Give the position of every malaria parasite and every leukocyte.
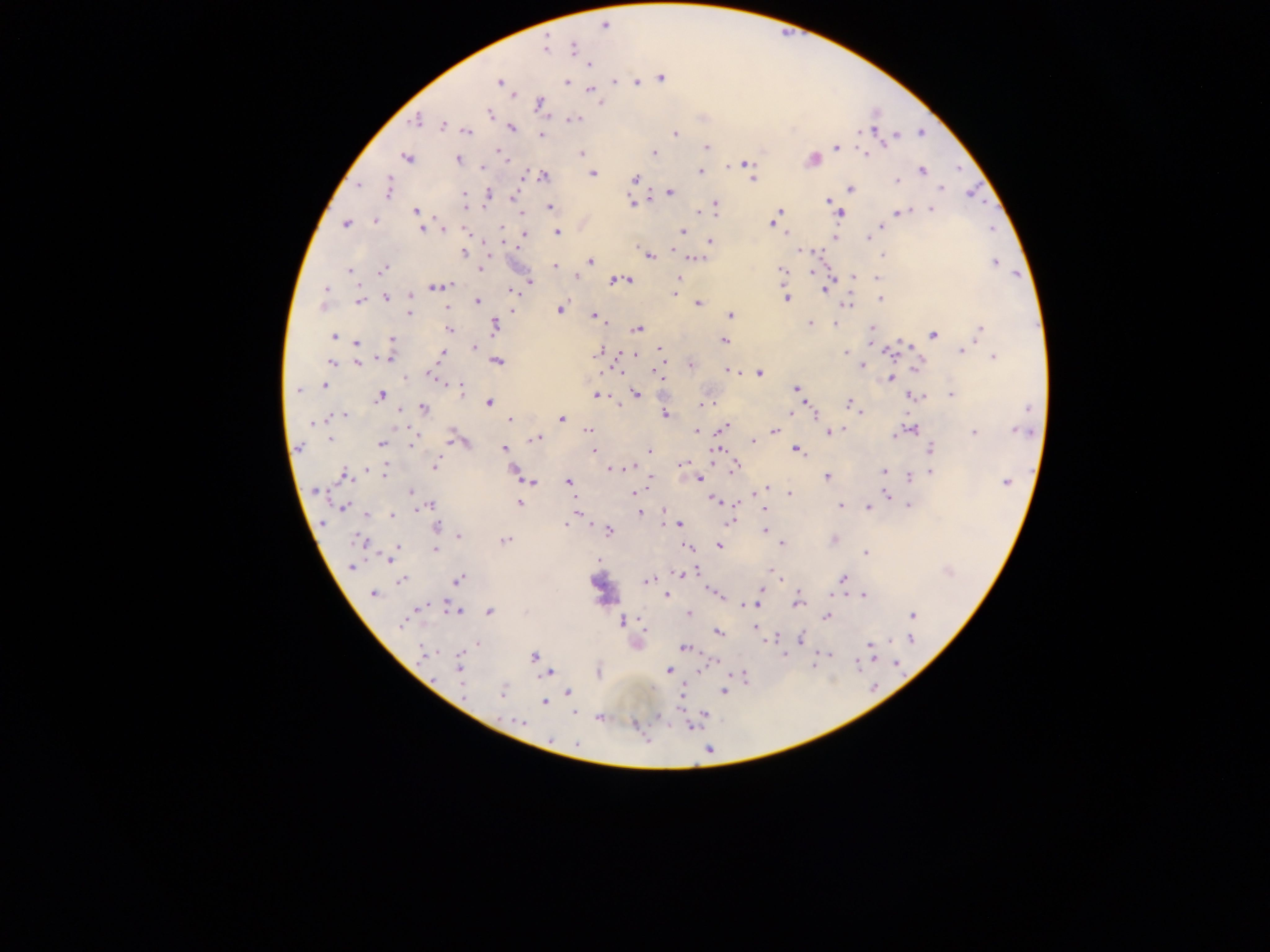
Approximate centers as x y in pixels.
Malaria parasites: 603 26; 546 48; 574 48; 590 64; 661 78; 499 82; 615 82; 639 82; 567 83; 592 91; 513 94; 539 103; 601 103; 489 113; 416 120; 572 120; 442 125; 512 128; 467 131; 921 133; 675 134; 541 136; 895 136; 706 147; 836 148; 500 153; 582 153; 654 153; 865 153; 505 157; 407 158; 457 159; 812 159; 507 161; 745 164; 482 168; 700 172; 921 172; 592 174; 544 177; 635 179; 751 179; 897 180; 359 184; 941 188; 387 189; 850 189; 670 192; 489 195; 465 196; 514 197; 827 201; 466 203; 632 203; 715 204; 550 207; 931 210; 417 211; 699 213; 900 213; 521 214; 778 214; 841 214; 375 221; 773 222; 346 224; 882 226; 502 228; 422 229; 444 230; 466 231; 683 231; 558 232; 524 234; 868 238; 835 239; 711 241; 801 251; 465 253; 883 255; 649 256; 695 258; 486 260; 589 261; 995 263; 556 266; 482 269; 383 270; 782 270; 350 271; 813 272; 576 277; 854 277; 678 278; 877 278; 625 279; 529 281; 614 281; 437 287; 327 288; 677 288; 825 289; 520 291; 416 292; 515 292; 410 296; 386 297; 787 298; 881 300; 359 301; 477 301; 698 304; 848 304; 322 306; 447 308; 560 309; 409 313; 730 315; 594 316; 602 322; 811 323; 835 324; 495 326; 449 329; 872 329; 981 329; 637 330; 933 335; 334 336; 392 338; 725 341; 356 343; 474 347; 660 349; 962 351; 599 352; 845 352; 442 354; 629 354; 635 354; 662 356; 390 357; 994 357; 498 361; 331 363; 358 363; 691 365; 862 366; 657 372; 730 372; 759 373; 430 377; 407 378; 891 379; 324 386; 461 388; 796 389; 298 390; 636 393; 951 395; 381 396; 598 396; 915 396; 489 403; 850 403; 702 405; 853 406; 424 408; 808 409; 399 411; 860 412; 790 413; 813 413; 665 414; 344 415; 560 419; 315 420; 510 420; 312 423; 724 428; 909 428; 774 430; 839 430; 587 431; 696 431; 1020 431; 830 432; 974 433; 450 437; 330 438; 536 438; 753 442; 381 444; 412 445; 299 447; 504 448; 931 449; 594 450; 717 450; 797 450; 649 451; 684 463; 435 466; 632 467; 735 467; 611 469; 513 471; 883 471; 932 473; 384 474; 345 476; 826 476; 650 478; 909 478; 700 479; 530 482; 1006 482; 568 483; 315 490; 765 490; 756 492; 410 493; 633 493; 789 493; 887 495; 714 499; 519 503; 429 505; 840 506; 908 506; 344 507; 422 507; 868 507; 764 510; 575 511; 640 513; 367 515; 392 515; 729 521; 566 524; 679 524; 437 526; 764 530; 609 531; 459 537; 360 540; 505 540; 834 540; 782 544; 719 546; 397 547; 687 547; 436 549; 865 554; 390 556; 351 567; 772 572; 679 573; 777 575; 459 579; 842 579; 402 580; 647 580; 761 591; 373 593; 864 595; 666 596; 797 603; 745 605; 756 605; 421 607; 458 611; 489 611; 689 613; 912 615; 826 617; 622 621; 401 624; 757 629; 718 633; 802 638; 910 639; 478 644; 870 645; 684 648; 423 653; 784 654; 827 655; 533 656; 896 664; 459 667; 668 670; 599 671; 548 673; 743 677; 463 685; 568 691; 723 691; 503 692; 682 693; 544 703; 575 714; 601 717; 521 722; 550 739; 577 744.
No leukocytes observed.

Image is 1270×952 pixels. Photographed through a microscope with a mobile-phone camera. Single field of view. Sample from Ghana. Thick blood film.